Name the blood parasite species.
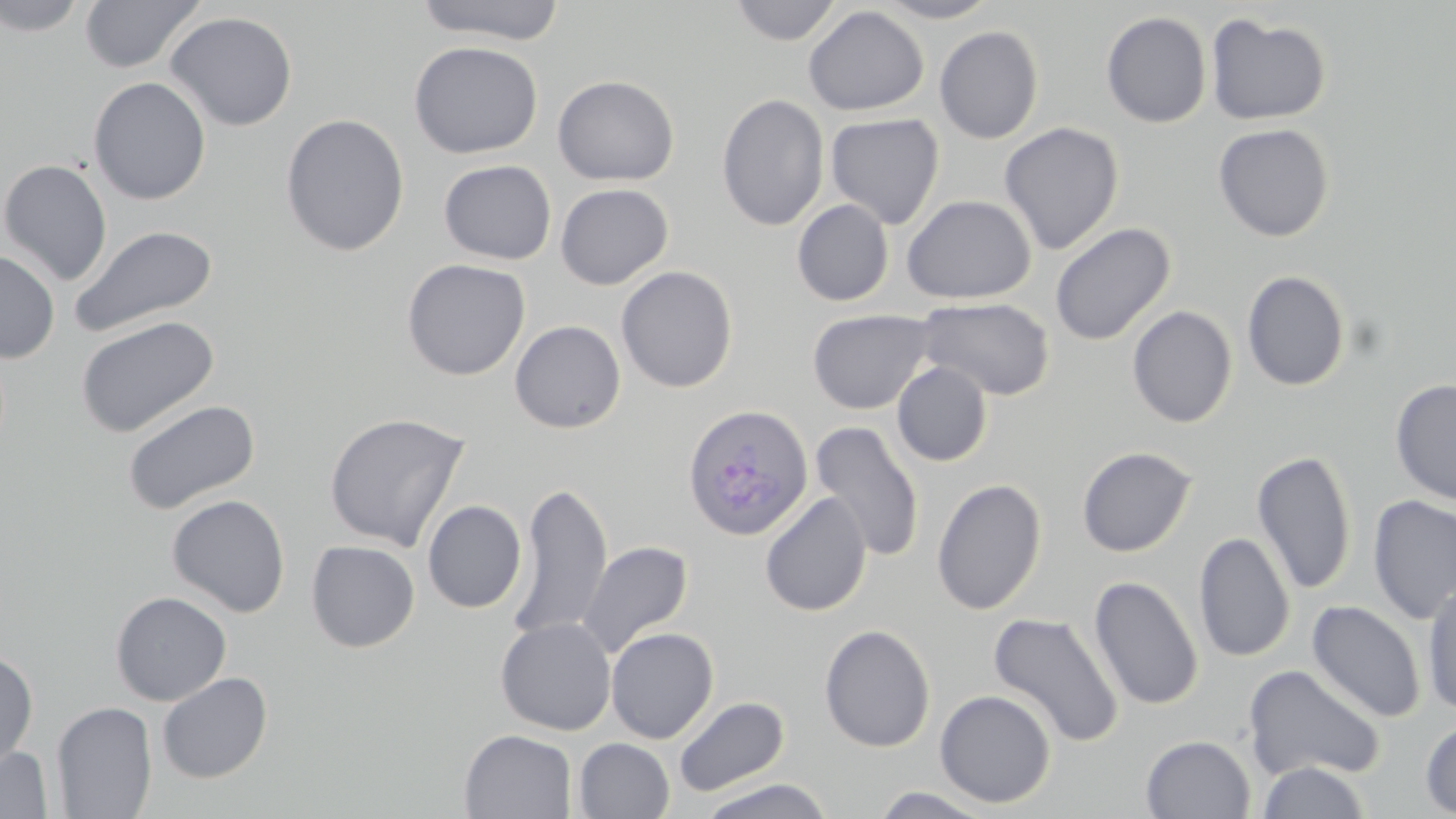

Plasmodium ovale.

Approximate bounding boxes as (x1, y1, x2, y2) in pixels. Plasmodium ovale-infected red blood cell locations: (685, 401, 816, 539). Uninfected red blood cell locations: (0, 0, 89, 37), (79, 0, 205, 74), (413, 0, 567, 45), (728, 0, 843, 46), (874, 0, 1000, 23), (803, 5, 929, 116), (164, 11, 298, 132), (1101, 11, 1212, 128), (1206, 13, 1332, 126), (934, 26, 1044, 144), (408, 40, 543, 159), (552, 75, 680, 186), (88, 76, 211, 205), (716, 93, 830, 232), (825, 112, 945, 229), (280, 113, 410, 257), (999, 122, 1124, 255), (1213, 123, 1334, 242), (0, 159, 113, 286), (438, 160, 557, 265), (555, 183, 674, 290), (901, 194, 1036, 304), (792, 199, 894, 306), (1050, 223, 1176, 346), (68, 224, 219, 339), (1, 249, 60, 363), (401, 258, 531, 381), (616, 265, 738, 394), (1241, 270, 1351, 391), (917, 297, 1055, 401), (1126, 305, 1238, 427), (808, 309, 936, 414), (75, 315, 219, 437), (509, 319, 627, 434), (892, 362, 993, 467), (1390, 379, 1456, 506), (121, 398, 260, 516), (324, 411, 470, 552), (809, 421, 926, 562), (1076, 446, 1197, 557), (1251, 449, 1357, 595), (931, 478, 1047, 616), (509, 482, 613, 640), (759, 491, 872, 617), (167, 494, 290, 617), (1368, 494, 1456, 625), (422, 500, 527, 613), (1193, 531, 1295, 664), (306, 540, 420, 652), (578, 540, 693, 658), (1089, 575, 1203, 711), (1422, 581, 1456, 715), (110, 591, 232, 706), (1307, 600, 1426, 723), (987, 611, 1125, 747), (495, 617, 616, 735), (819, 624, 936, 752), (605, 626, 719, 743), (0, 648, 38, 771), (1243, 664, 1386, 784), (156, 671, 273, 784), (934, 689, 1056, 808), (673, 696, 789, 797), (52, 701, 157, 819), (1420, 717, 1456, 817), (459, 729, 577, 818), (1141, 734, 1256, 818), (574, 738, 675, 819), (0, 744, 54, 818), (1256, 761, 1371, 818), (695, 777, 837, 819), (869, 785, 998, 818). May-Grünwald-Giemsa stain. Light microscopy. Image is 1456×819 pixels. Thin blood smear. Single field of view. 1000x magnification.